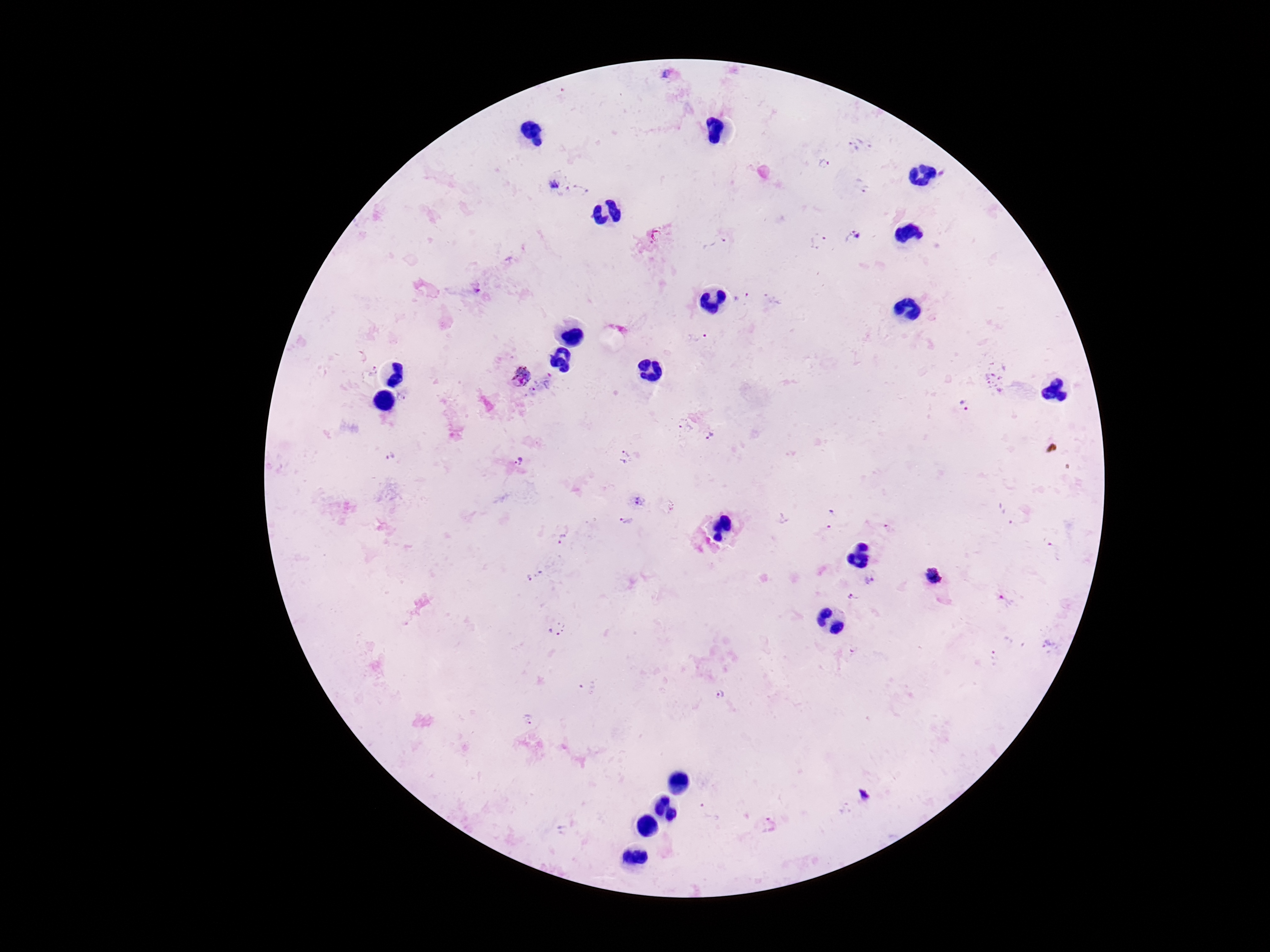
{
  "plasmodium_parasite_locations": "approximate centers as [x, y] in pixels: [853, 147], [824, 164], [555, 184], [861, 186], [853, 236], [818, 241], [477, 288], [696, 337], [520, 375], [551, 382], [533, 391], [965, 406], [685, 425], [710, 437], [390, 457], [624, 457], [519, 461], [639, 501], [626, 520], [562, 539], [1054, 550], [534, 575], [933, 577], [869, 581], [854, 598], [556, 629], [587, 686], [719, 695], [528, 720], [768, 824]",
  "image_size": "1270×952 pixels",
  "magnification": "100x",
  "patient_malaria_status": "positive",
  "capture": "smartphone camera through the microscope eyepiece",
  "preparation": "thick blood smear",
  "field_of_view": "single",
  "stain": "Giemsa"
}